Report the malaria status of this cell.
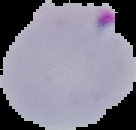

It is parasitized.

Summary:
  - Preparation: thin blood film
  - Image size: 136×130 pixels
  - Image type: cell region segmented out of the field of view; surrounding area masked to black